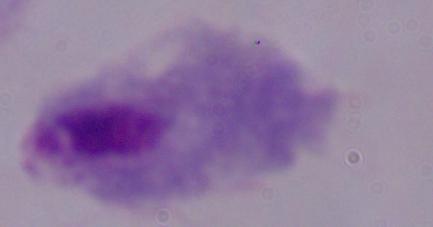
Photomicrograph. A trichomonad is shown. Captured at 1000x magnification.